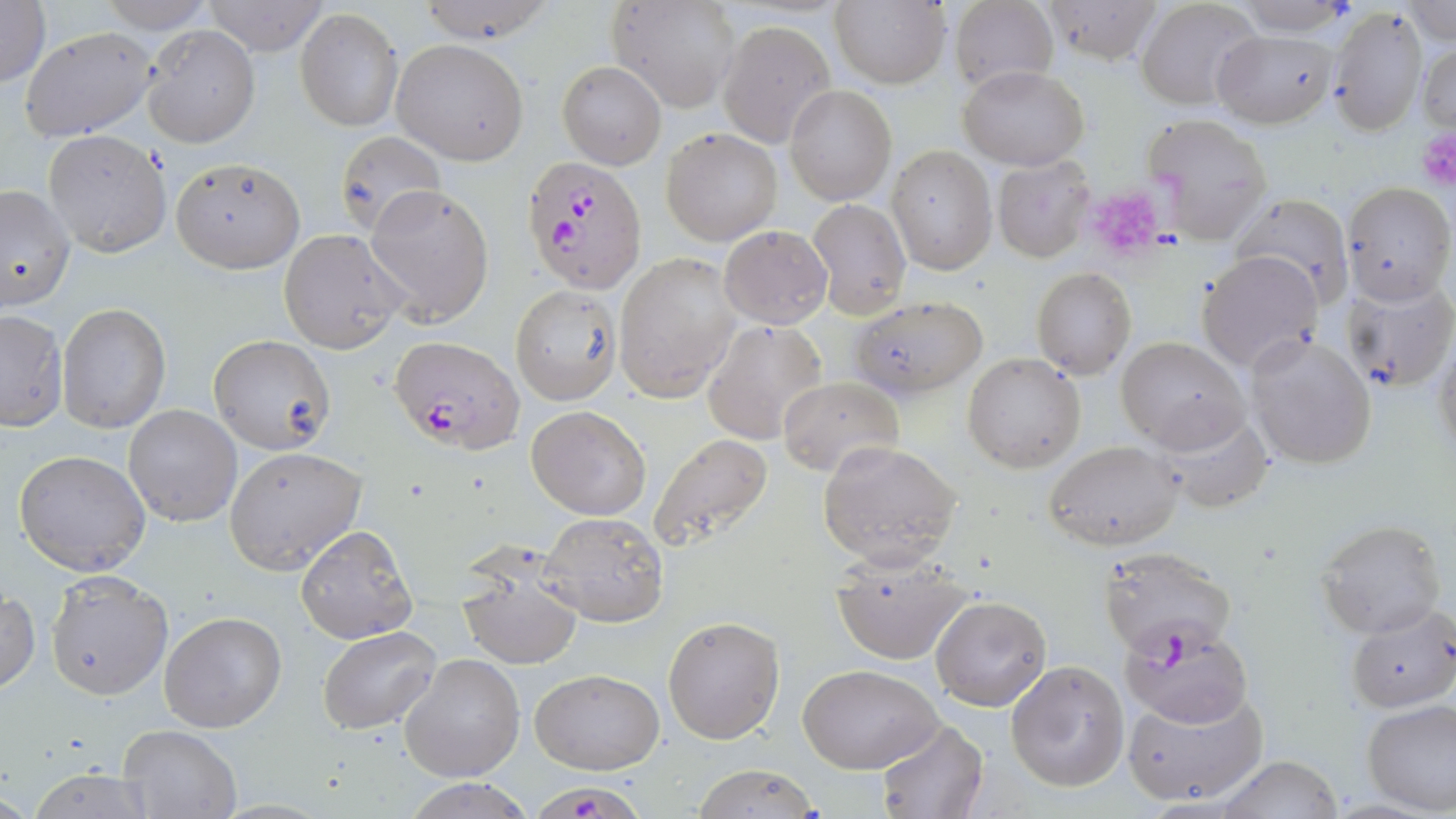 Approximate bounding boxes as (x1,y1)-(x2,y2) corner pairs in pixels. Plasmodium falciparum-infected red blood cell locations: (521,154)-(647,291), (391,336)-(523,452), (1097,544)-(1237,659), (539,785)-(647,818). Uninfected red blood cell locations: (1,0)-(50,88), (95,0)-(218,34), (200,0)-(331,57), (413,0)-(560,44), (607,0)-(741,113), (950,0)-(1057,93), (1041,0)-(1165,65), (1135,0)-(1262,111), (1231,0)-(1353,36), (830,1)-(950,88), (1403,1)-(1455,46), (1327,4)-(1428,137), (295,8)-(402,132), (718,19)-(834,146), (142,24)-(259,148), (20,27)-(159,141), (1213,29)-(1338,128), (392,39)-(529,164), (1418,40)-(1455,137), (558,63)-(665,168), (960,65)-(1088,169), (784,84)-(897,205), (1143,113)-(1273,244), (661,127)-(782,245), (43,130)-(171,259), (333,130)-(444,237), (887,146)-(997,275), (990,156)-(1095,263), (170,157)-(305,273), (0,180)-(76,313), (1342,182)-(1455,304), (364,183)-(495,326), (1231,191)-(1354,306), (807,198)-(911,319), (719,225)-(832,328), (278,228)-(409,354), (1197,251)-(1323,373), (617,252)-(740,401), (1031,268)-(1138,378), (1007,273)-(1119,448), (1341,276)-(1456,394), (510,288)-(618,404), (851,295)-(989,404), (57,301)-(171,435), (0,308)-(68,431), (700,319)-(828,444), (1431,330)-(1456,470), (1245,332)-(1379,469), (209,336)-(334,454), (1117,336)-(1249,449), (962,353)-(1086,473), (778,375)-(904,478), (123,404)-(242,528), (1147,404)-(1275,515), (525,406)-(652,519), (649,434)-(773,550), (1044,439)-(1183,552), (818,440)-(962,568), (224,446)-(366,574), (13,450)-(151,575), (539,511)-(668,627), (1316,518)-(1447,640), (296,525)-(417,643), (828,548)-(970,665), (456,560)-(585,670), (44,570)-(173,701), (1,589)-(40,695), (930,595)-(1052,711), (1344,601)-(1456,714), (159,610)-(289,733), (661,613)-(785,744), (1118,620)-(1255,729), (317,626)-(441,734), (400,653)-(525,780), (1005,660)-(1128,792), (799,663)-(943,774), (531,668)-(664,775), (1120,683)-(1270,809), (1361,700)-(1456,817), (875,718)-(990,819), (116,724)-(241,818), (1214,755)-(1345,819), (23,765)-(160,819), (688,767)-(822,819), (401,777)-(532,817). Platelet locations: (1414,127)-(1456,193), (1078,187)-(1161,263). Slide-level diagnosis: Plasmodium falciparum. One field of a larger specimen. May-Grünwald-Giemsa stain. Image is 1456×819 pixels. Light microscopy. Captured at 1000x magnification. Thin blood film.